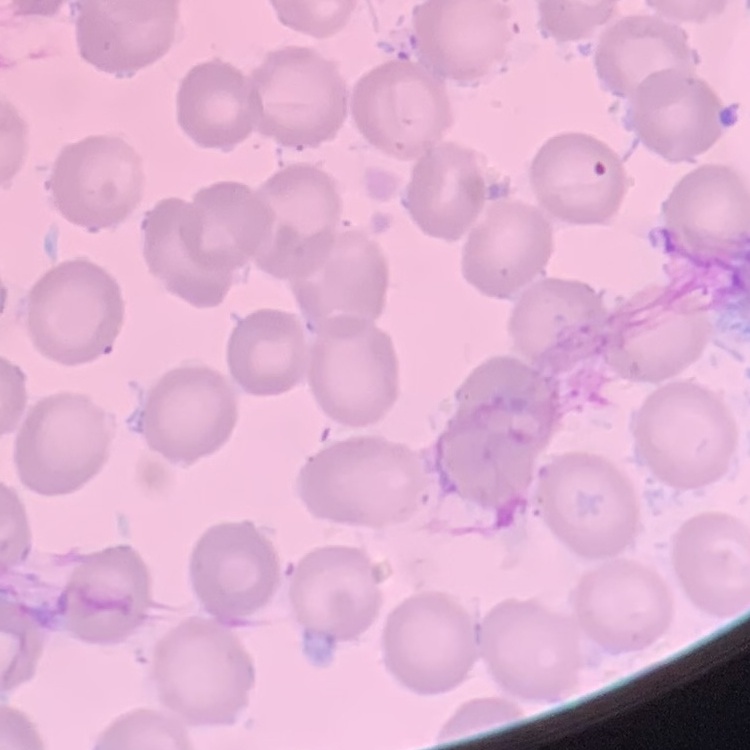

erythrocyte morphology = no rouleaux formation
image type = square crop of a larger photomicrograph
stain = Field's or Giemsa
preparation = thin blood film